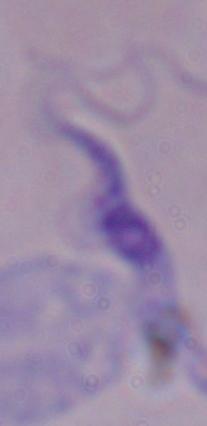
Micrograph. Captured at 1000x magnification. A trypanosome is shown.